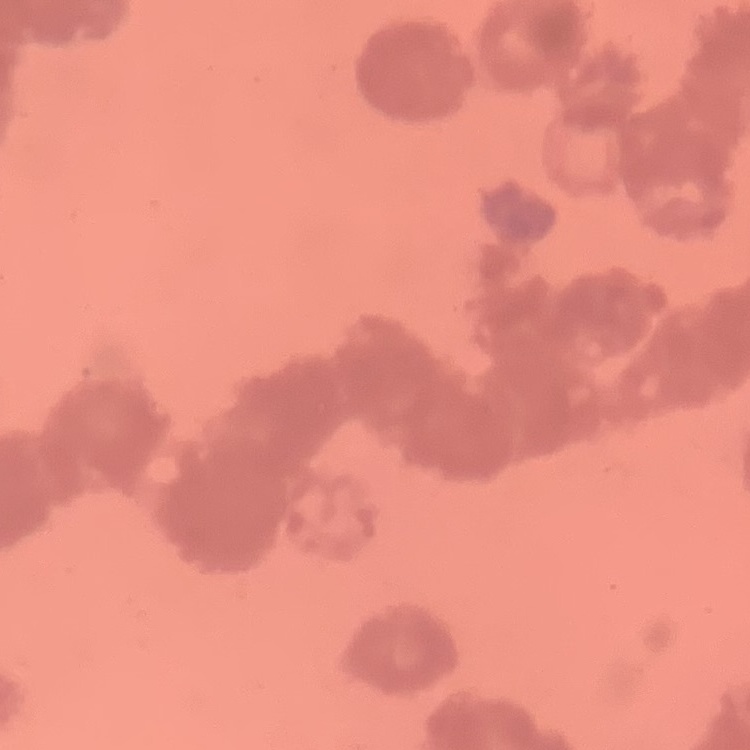
red blood cell morphology = rouleaux formation
image type = one tile cut from a larger photomicrograph
preparation = thin blood smear
stain = Field's or Giemsa